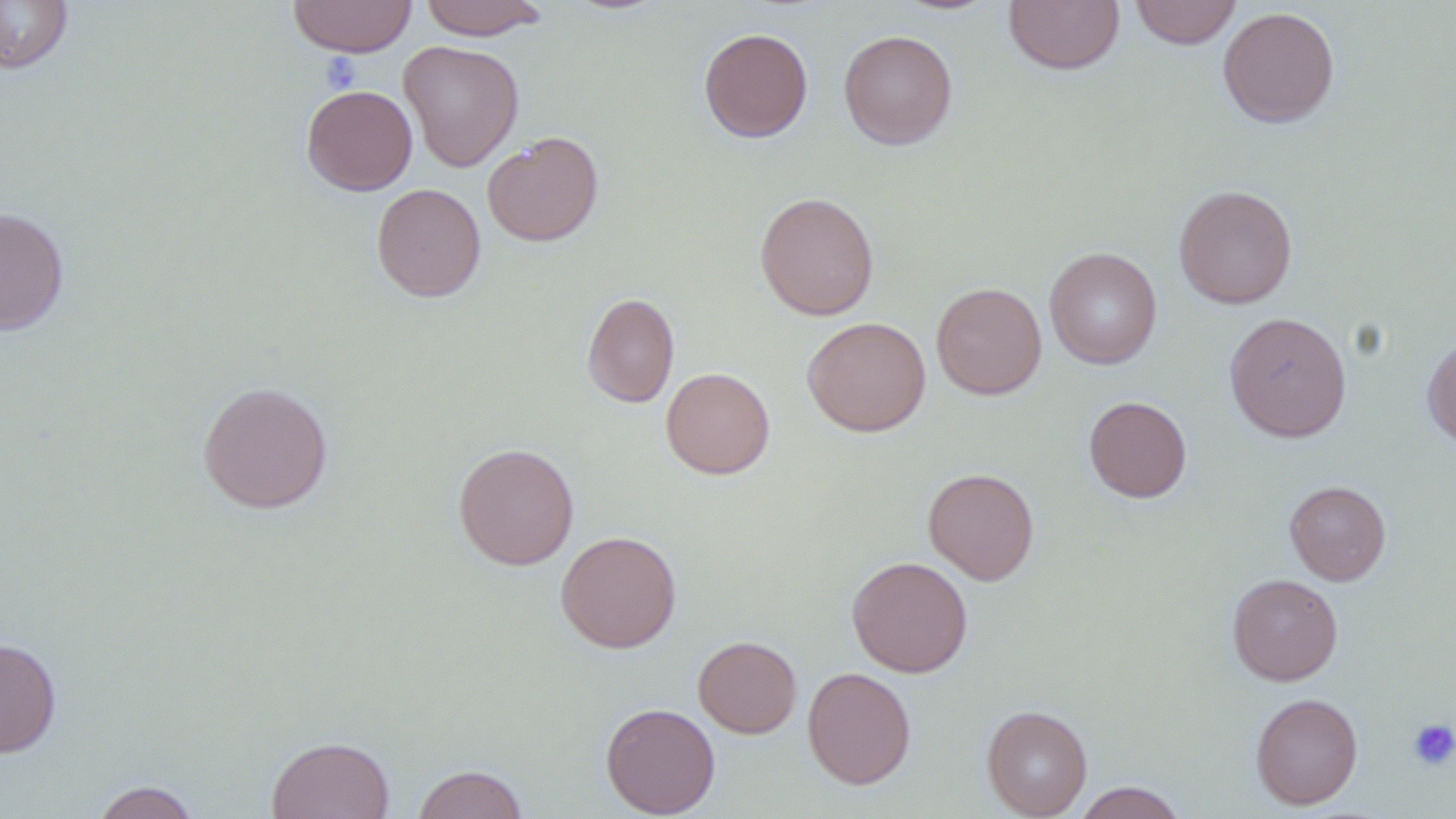

Summary:
  - Coordinate format: approximate bounding boxes as named x1/y1/x2/y2 corners in pixels
  - Uninfected red blood cell locations: (x1=287, y1=0, x2=417, y2=58), (x1=418, y1=0, x2=549, y2=40), (x1=1004, y1=0, x2=1124, y2=75), (x1=1129, y1=0, x2=1242, y2=49), (x1=0, y1=1, x2=74, y2=74), (x1=892, y1=1, x2=1002, y2=16), (x1=1217, y1=6, x2=1340, y2=129), (x1=698, y1=27, x2=813, y2=143), (x1=839, y1=30, x2=957, y2=150), (x1=398, y1=40, x2=524, y2=172), (x1=301, y1=85, x2=418, y2=195), (x1=482, y1=131, x2=603, y2=246), (x1=371, y1=182, x2=486, y2=303), (x1=1173, y1=184, x2=1297, y2=309), (x1=754, y1=191, x2=879, y2=320), (x1=0, y1=206, x2=69, y2=335), (x1=1044, y1=247, x2=1162, y2=369), (x1=931, y1=282, x2=1046, y2=399), (x1=582, y1=292, x2=679, y2=408), (x1=1224, y1=312, x2=1352, y2=441), (x1=802, y1=316, x2=931, y2=437), (x1=1422, y1=336, x2=1456, y2=449), (x1=661, y1=367, x2=775, y2=479), (x1=197, y1=380, x2=332, y2=513), (x1=1083, y1=396, x2=1192, y2=502), (x1=453, y1=442, x2=579, y2=570), (x1=923, y1=467, x2=1039, y2=585), (x1=1285, y1=480, x2=1391, y2=584), (x1=555, y1=530, x2=682, y2=653), (x1=846, y1=556, x2=973, y2=678), (x1=1227, y1=573, x2=1343, y2=685), (x1=693, y1=635, x2=801, y2=738), (x1=0, y1=638, x2=62, y2=758), (x1=803, y1=666, x2=916, y2=790), (x1=1250, y1=692, x2=1363, y2=810), (x1=600, y1=702, x2=720, y2=818), (x1=981, y1=704, x2=1092, y2=818), (x1=266, y1=735, x2=394, y2=819), (x1=413, y1=764, x2=528, y2=819), (x1=90, y1=780, x2=201, y2=819), (x1=1072, y1=782, x2=1187, y2=819)
  - Platelet locations: (x1=319, y1=52, x2=362, y2=92), (x1=1407, y1=718, x2=1456, y2=771)
  - Slide-level diagnosis: negative for blood parasites
  - Image size: 1456×819 pixels
  - Modality: optical microscopy
  - Stain: May-Grünwald-Giemsa
  - Magnification: 1000x
  - Field of view: one of a larger specimen
  - Preparation: thin blood film